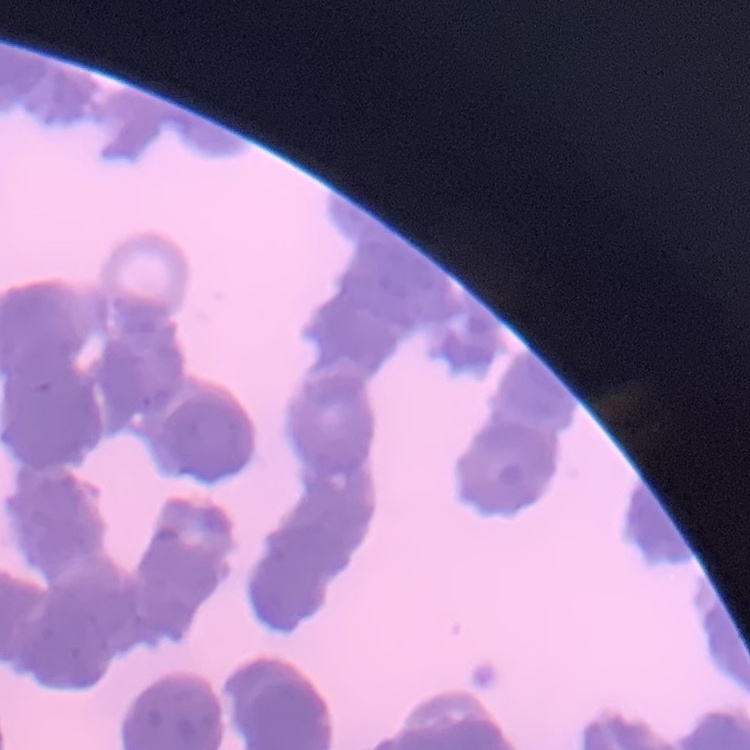
{
  "erythrocyte_morphology": "rouleaux formation",
  "preparation": "thin blood smear",
  "stain": "Field's or Giemsa",
  "image_type": "square crop of a larger photomicrograph"
}